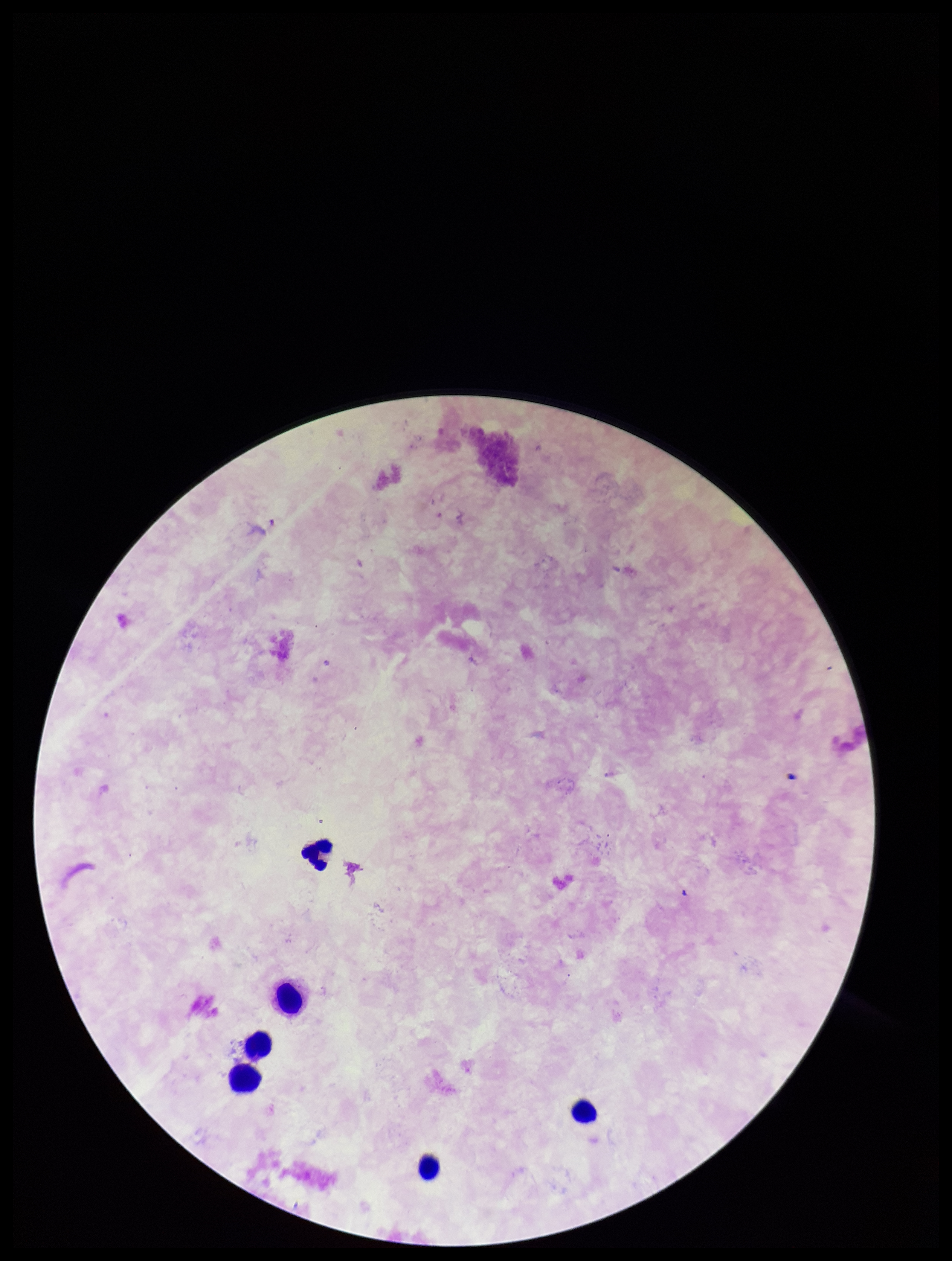
Summary:
  - Preparation: thick smear
  - Stain: Giemsa
  - Leukocyte count: 6
  - Field of view: one from this slide
  - Plasmodium parasites: none identified
  - Image size: 952×1261 pixels
  - Parasite count: 0
  - Patient malaria status: negative
  - Capture: smartphone photograph through the microscope eyepiece